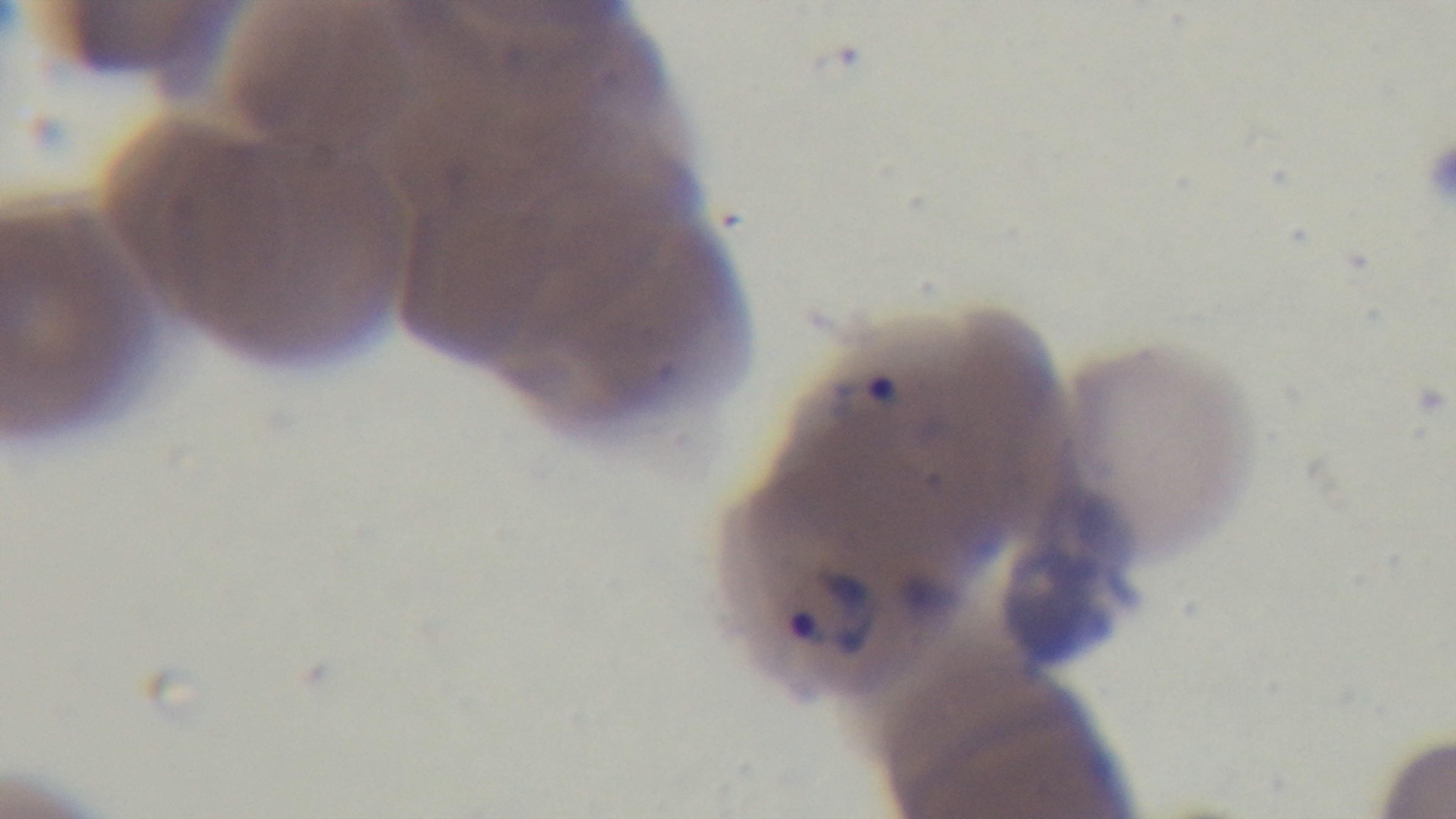

Summary:
  - Capture: mounted 4K digital camera
  - Malaria status: positive
  - Stain: Giemsa
  - Field of view: single
  - Preparation: thin blood film
  - Modality: light microscopy
  - Objective: 100x oil immersion